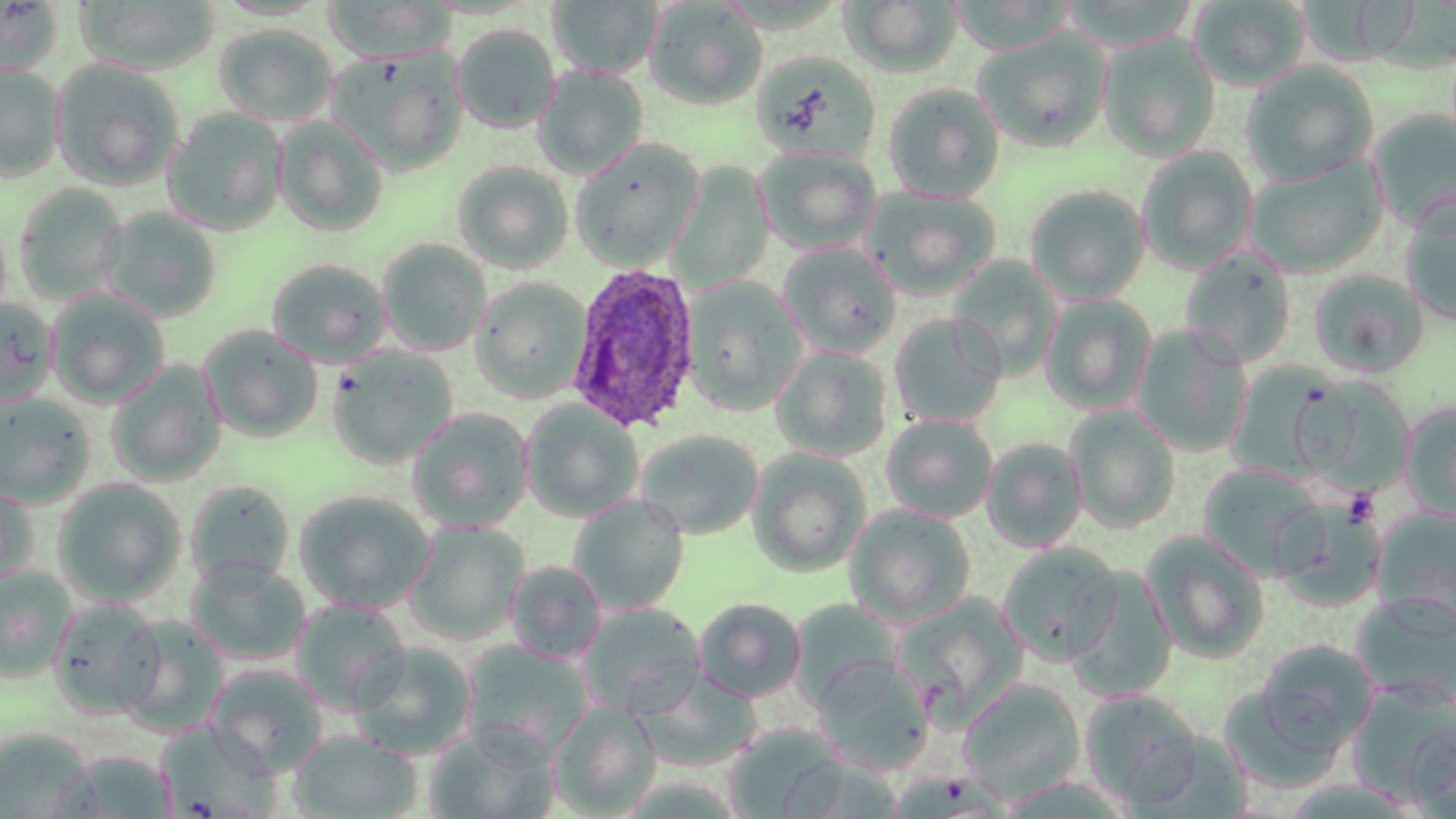 Approximate bounding boxes as [x1, y1, x2, y2] in pixels. Uninfected red blood cell locations: [74, 0, 221, 73], [322, 0, 457, 65], [547, 0, 662, 78], [644, 0, 768, 110], [841, 0, 963, 77], [1188, 0, 1311, 90], [0, 1, 64, 76], [213, 23, 338, 126], [451, 23, 560, 134], [975, 28, 1112, 151], [1098, 33, 1221, 160], [329, 46, 468, 172], [751, 51, 881, 162], [51, 57, 184, 191], [1241, 61, 1379, 183], [0, 62, 66, 182], [533, 65, 649, 179], [882, 83, 1005, 202], [162, 109, 288, 235], [1368, 110, 1456, 233], [275, 117, 389, 237], [569, 140, 702, 271], [755, 145, 882, 254], [1136, 146, 1258, 272], [1244, 156, 1388, 277], [453, 161, 574, 274], [668, 163, 775, 293], [14, 183, 129, 305], [1024, 184, 1152, 303], [864, 186, 1002, 300], [1399, 199, 1456, 325], [100, 207, 223, 322], [377, 240, 491, 357], [778, 242, 902, 357], [1179, 246, 1299, 368], [947, 256, 1062, 378], [265, 258, 392, 368], [1307, 269, 1428, 378], [472, 277, 592, 403], [681, 277, 805, 413], [46, 289, 170, 406], [1040, 294, 1157, 413], [0, 298, 59, 409], [890, 312, 1005, 428], [197, 325, 324, 443], [1131, 325, 1252, 456], [326, 346, 459, 468], [772, 347, 894, 461], [107, 361, 226, 486], [1228, 364, 1354, 490], [1293, 374, 1417, 496], [0, 392, 96, 509], [520, 400, 645, 522], [1400, 402, 1456, 522], [1066, 405, 1182, 533], [406, 408, 534, 532], [881, 414, 999, 523], [634, 429, 765, 540], [982, 437, 1088, 552], [747, 448, 871, 577], [1197, 463, 1327, 581], [53, 478, 187, 607], [185, 480, 295, 590], [0, 484, 38, 589], [293, 490, 436, 614], [568, 494, 689, 615], [1270, 496, 1387, 611], [844, 504, 977, 626], [1371, 507, 1456, 631], [404, 521, 528, 644], [1140, 531, 1271, 663], [997, 543, 1124, 664], [185, 558, 311, 666], [505, 560, 607, 664], [0, 566, 77, 681], [1351, 592, 1456, 710], [893, 593, 1030, 727], [48, 597, 165, 718], [693, 597, 807, 702], [790, 598, 902, 707], [291, 600, 410, 714], [577, 602, 705, 717], [115, 615, 228, 736], [460, 638, 594, 760], [1249, 640, 1378, 760], [350, 642, 478, 760], [811, 654, 935, 776], [205, 664, 328, 775], [634, 669, 762, 770], [957, 678, 1086, 801], [1347, 684, 1456, 805], [1080, 689, 1204, 808], [550, 702, 662, 817], [155, 721, 281, 818], [1406, 723, 1456, 819], [423, 725, 559, 819], [722, 725, 851, 817], [0, 728, 94, 819], [288, 730, 422, 818], [1121, 733, 1255, 819], [55, 750, 177, 817]. Plasmodium ovale-infected red blood cell locations: [567, 262, 701, 432]. Slide-level diagnosis: Plasmodium ovale. May-Grünwald-Giemsa stain. 1000x magnification. Image is 1456×819 pixels. One field of a larger specimen. Thin blood film. Optical microscopy.